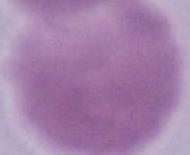

Summary:
  - Identification: erythrocyte
  - Magnification: 1000x
  - Modality: photomicrograph